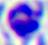

identification = white blood cell
modality = micrograph
magnification = 400x